Locate every Plasmodium vivax-infected red blood cell.
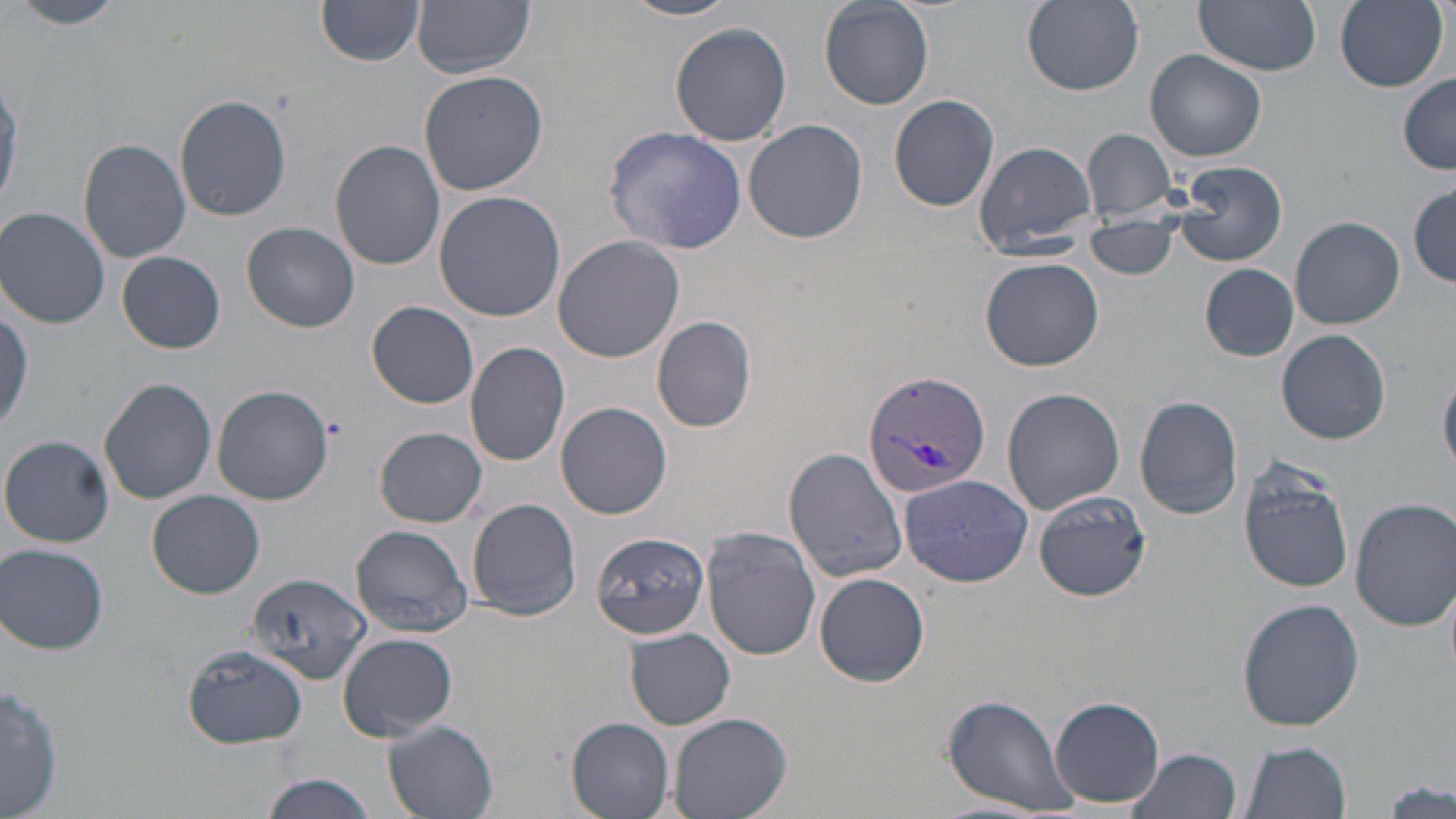
Approximate bounding boxes as (x1,y1)-(x2,y2) corner pairs in pixels.
Plasmodium vivax-infected red blood cells: (863,369)-(990,501).

Uninfected red blood cell locations: (11,0)-(126,29), (316,0)-(427,66), (413,0)-(534,77), (621,0)-(739,22), (818,0)-(934,110), (1022,0)-(1144,93), (1197,0)-(1322,75), (1334,0)-(1446,91), (670,21)-(792,146), (1146,50)-(1267,163), (419,69)-(550,196), (0,72)-(22,215), (1399,76)-(1456,173), (888,94)-(1000,212), (174,95)-(292,221), (745,119)-(867,243), (604,125)-(747,254), (1082,128)-(1178,221), (79,139)-(191,262), (330,139)-(445,270), (973,140)-(1098,254), (1171,161)-(1288,267), (1409,186)-(1456,286), (433,190)-(566,321), (1,207)-(110,328), (1290,217)-(1405,329), (1084,218)-(1179,279), (243,222)-(361,332), (551,235)-(687,363), (117,252)-(225,354), (981,256)-(1105,372), (1201,263)-(1299,359), (0,300)-(34,435), (367,300)-(479,409), (652,316)-(757,433), (1278,328)-(1391,444), (466,342)-(571,467), (1439,369)-(1456,474), (98,378)-(217,503), (211,386)-(332,504), (1001,387)-(1125,514), (1135,395)-(1243,520), (556,401)-(672,519), (375,426)-(487,527), (2,435)-(115,547), (784,448)-(909,581), (1236,461)-(1355,593), (899,472)-(1034,587), (1031,489)-(1154,602), (148,490)-(265,598), (1351,495)-(1456,633), (466,497)-(581,621), (350,524)-(475,638), (702,527)-(822,658), (588,533)-(709,642), (1,543)-(110,654), (249,572)-(370,682), (816,572)-(930,686), (1237,598)-(1365,731), (625,628)-(735,730), (339,632)-(458,741), (181,643)-(310,748), (1,682)-(62,819), (941,693)-(1075,815), (1049,694)-(1165,808), (669,712)-(792,819), (567,717)-(675,818), (383,719)-(499,818), (1239,739)-(1352,819), (1128,747)-(1243,819), (258,772)-(380,819), (1380,777)-(1454,819). Slide-level diagnosis: Plasmodium vivax. Image is 1456×819 pixels. May-Grünwald-Giemsa stain. Optical microscopy. Thin blood film. 1000x magnification. One field of a larger specimen.